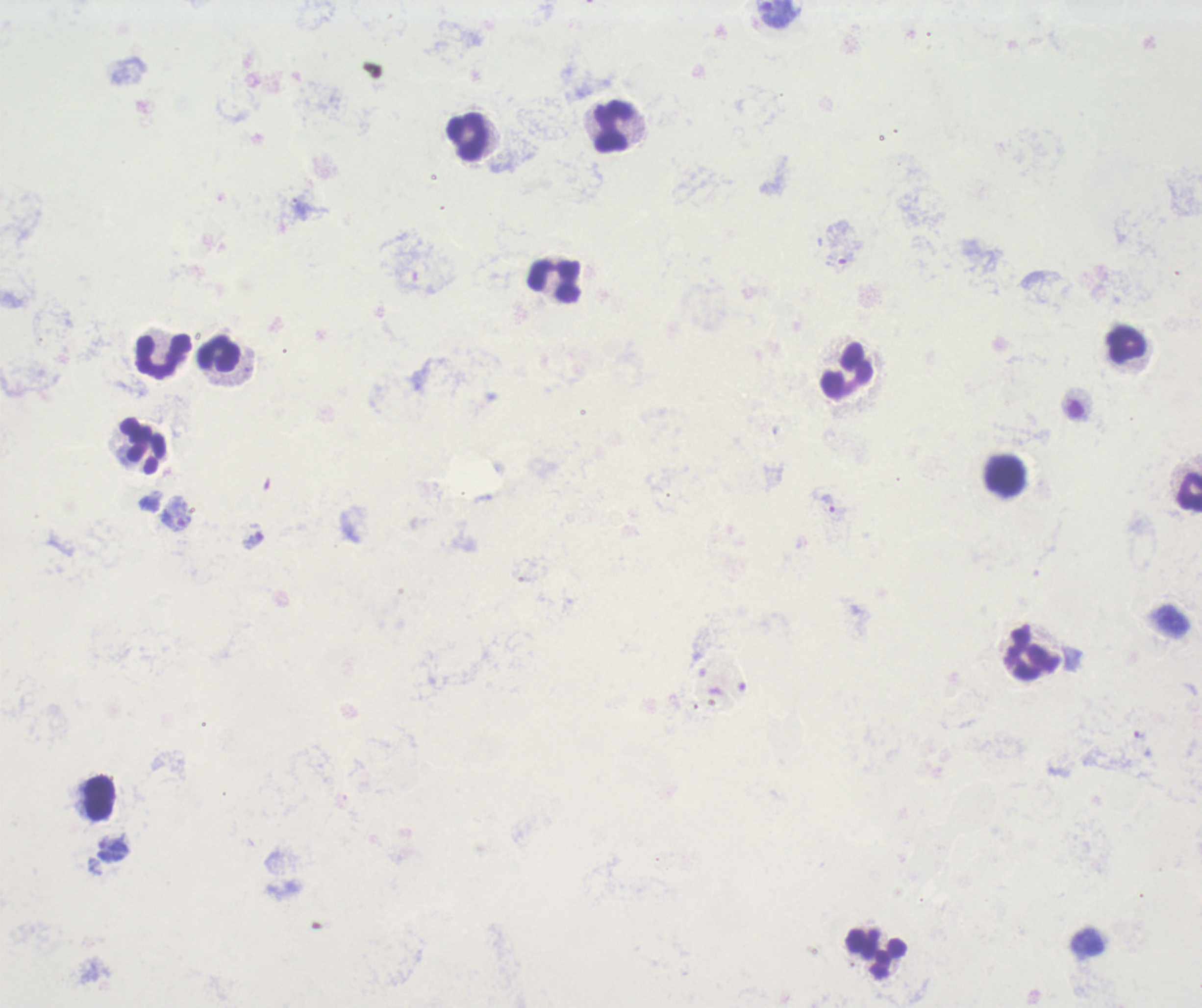

Approximate centers as [x, y] in pixels. Trophozoite locations: [840, 259], [828, 503], [1140, 735]. Leukocyte locations: [612, 127], [468, 139], [554, 280], [1124, 345], [217, 350], [162, 356], [846, 370], [142, 445], [1005, 477], [1189, 491], [1031, 654], [98, 796], [876, 953]. Image is 1202×1008 pixels. Background quality: poor. Result: positive for malaria parasites. Captured at 100x magnification. Thick blood smear. Romanowsky stain. Single field of view. Previously used in an actual diagnosis.